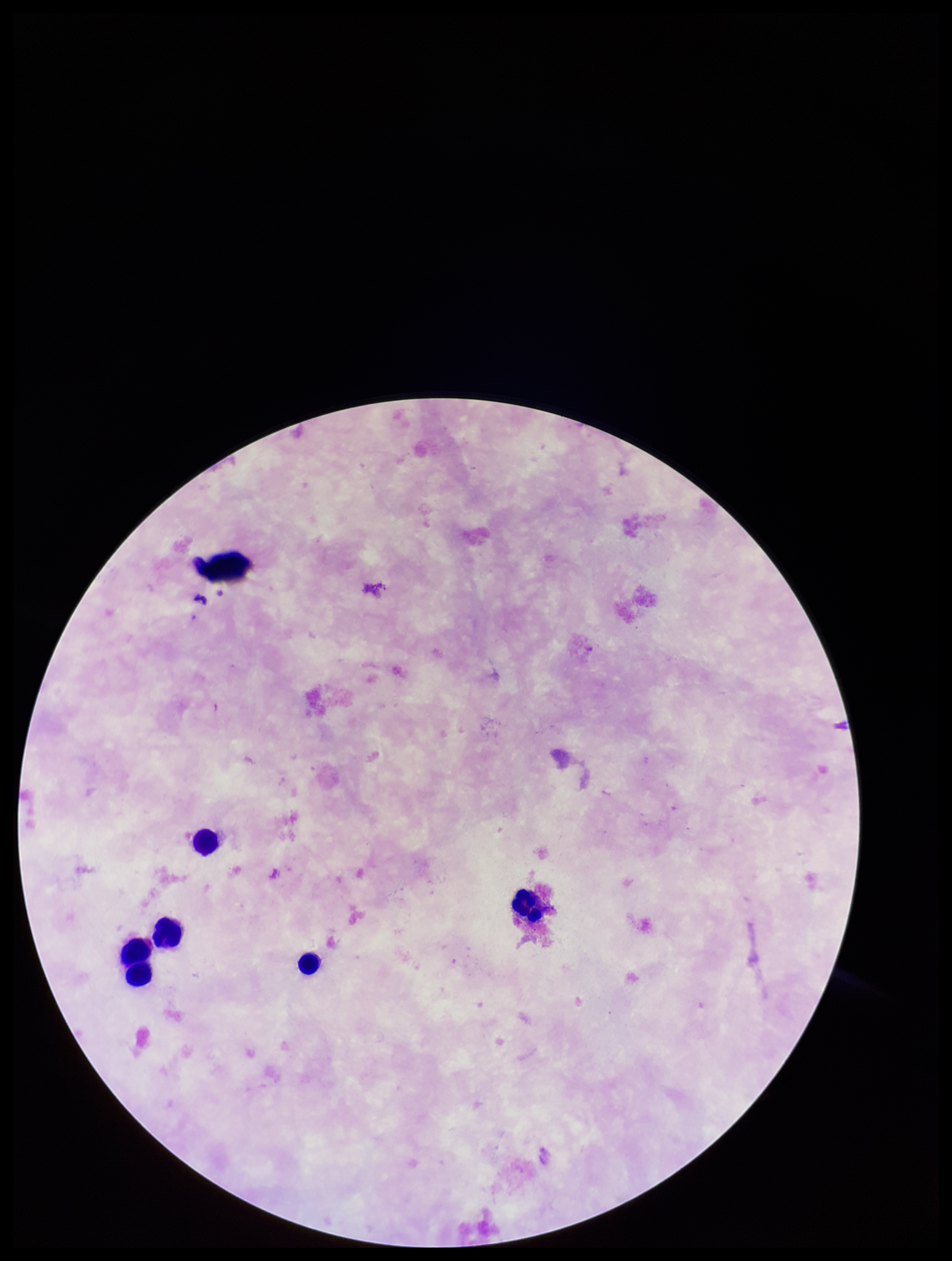
Summary:
  - Patient malaria status: negative
  - Preparation: thick
  - Image size: 952×1261 pixels
  - Capture: smartphone photograph through the microscope eyepiece
  - Plasmodium parasites: none detected
  - Field of view: single
  - Stain: Giemsa
  - Leukocyte count: 6
  - Parasite count: 0